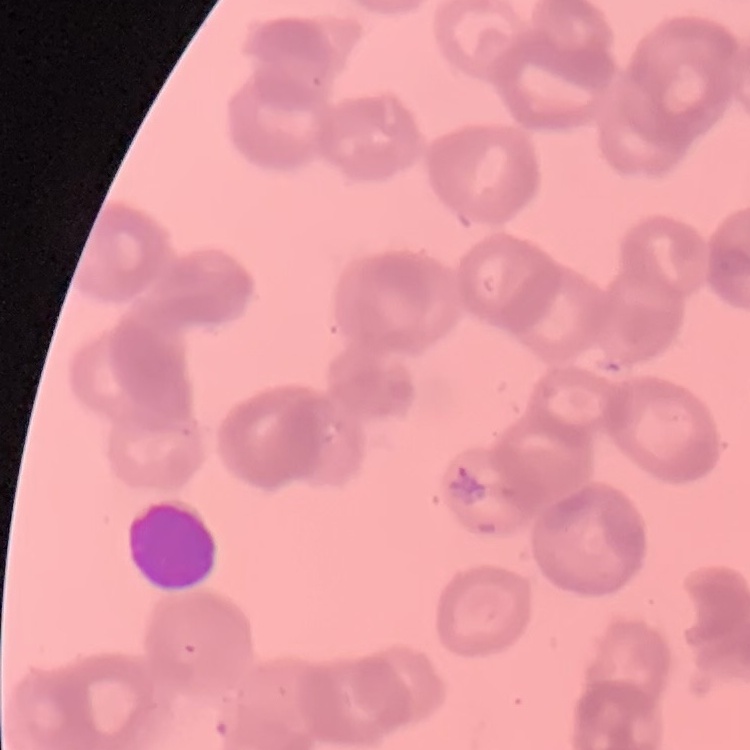

Summary:
  - Red blood cell morphology: rouleaux formation
  - Image type: square crop of a larger photomicrograph
  - Preparation: thin peripheral smear
  - Stain: Field's or Giemsa